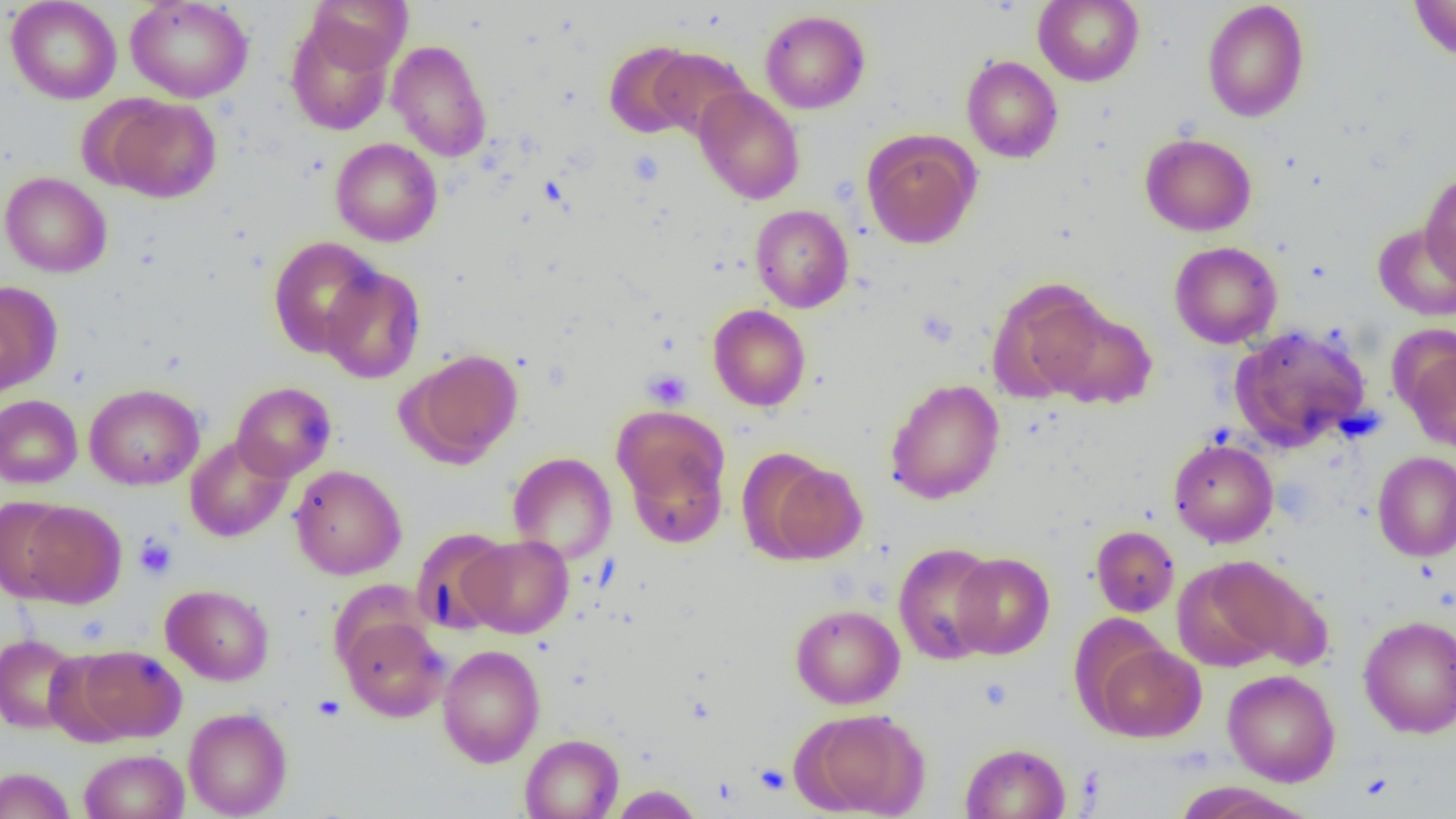
Summary:
  - Coordinate format: approximate bounding boxes as (x1,y1)-(x2,y2) corner pairs in pixels
  - Uninfected red blood cell locations: (6,0)-(121,104), (125,0)-(253,103), (307,0)-(412,73), (1033,0)-(1144,86), (1409,0)-(1456,61), (1201,1)-(1310,123), (759,10)-(871,114), (285,18)-(394,136), (387,39)-(492,161), (604,40)-(700,139), (650,47)-(751,140), (961,55)-(1063,163), (694,86)-(805,204), (99,95)-(222,203), (862,129)-(980,249), (1140,133)-(1256,236), (330,138)-(442,247), (1420,170)-(1456,284), (0,171)-(112,277), (750,204)-(853,313), (1372,222)-(1456,322), (267,235)-(383,358), (1170,241)-(1282,348), (320,265)-(426,384), (988,278)-(1110,402), (0,282)-(60,398), (708,304)-(811,411), (1044,305)-(1157,409), (1229,324)-(1372,451), (1399,342)-(1456,453), (403,349)-(524,466), (885,378)-(1004,504), (231,381)-(337,481), (84,383)-(204,490), (0,394)-(82,488), (616,416)-(731,548), (184,435)-(293,543), (1168,439)-(1278,547), (1372,451)-(1456,562), (507,452)-(617,563), (754,456)-(868,565), (290,464)-(406,580), (0,496)-(76,602), (16,500)-(126,608), (1091,525)-(1179,617), (411,528)-(513,634), (462,535)-(573,638), (893,542)-(1001,665), (950,552)-(1055,659), (1188,555)-(1328,671), (161,584)-(274,686), (790,604)-(905,709), (339,615)-(449,722), (1358,615)-(1456,738), (0,634)-(83,734), (1089,641)-(1207,742), (437,644)-(545,768), (72,645)-(187,742), (1223,669)-(1340,786), (183,707)-(292,818), (798,709)-(929,818), (520,734)-(623,818), (960,742)-(1071,819), (79,749)-(189,819), (0,767)-(76,819), (1170,782)-(1317,818), (608,785)-(704,818)
  - Platelet locations: (626,148)-(665,188), (643,369)-(692,409), (134,534)-(177,580), (312,694)-(347,721), (755,764)-(791,794)
  - Slide-level diagnosis: negative for blood parasites
  - Preparation: thin blood smear
  - Modality: light microscopy
  - Magnification: 1000x
  - Image size: 1456×819 pixels
  - Field of view: one of a larger specimen